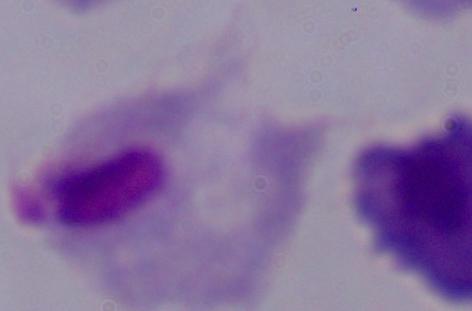

Summary:
  - Identification: trichomonad
  - Modality: photomicrograph
  - Magnification: 1000x